State the blood parasite species.
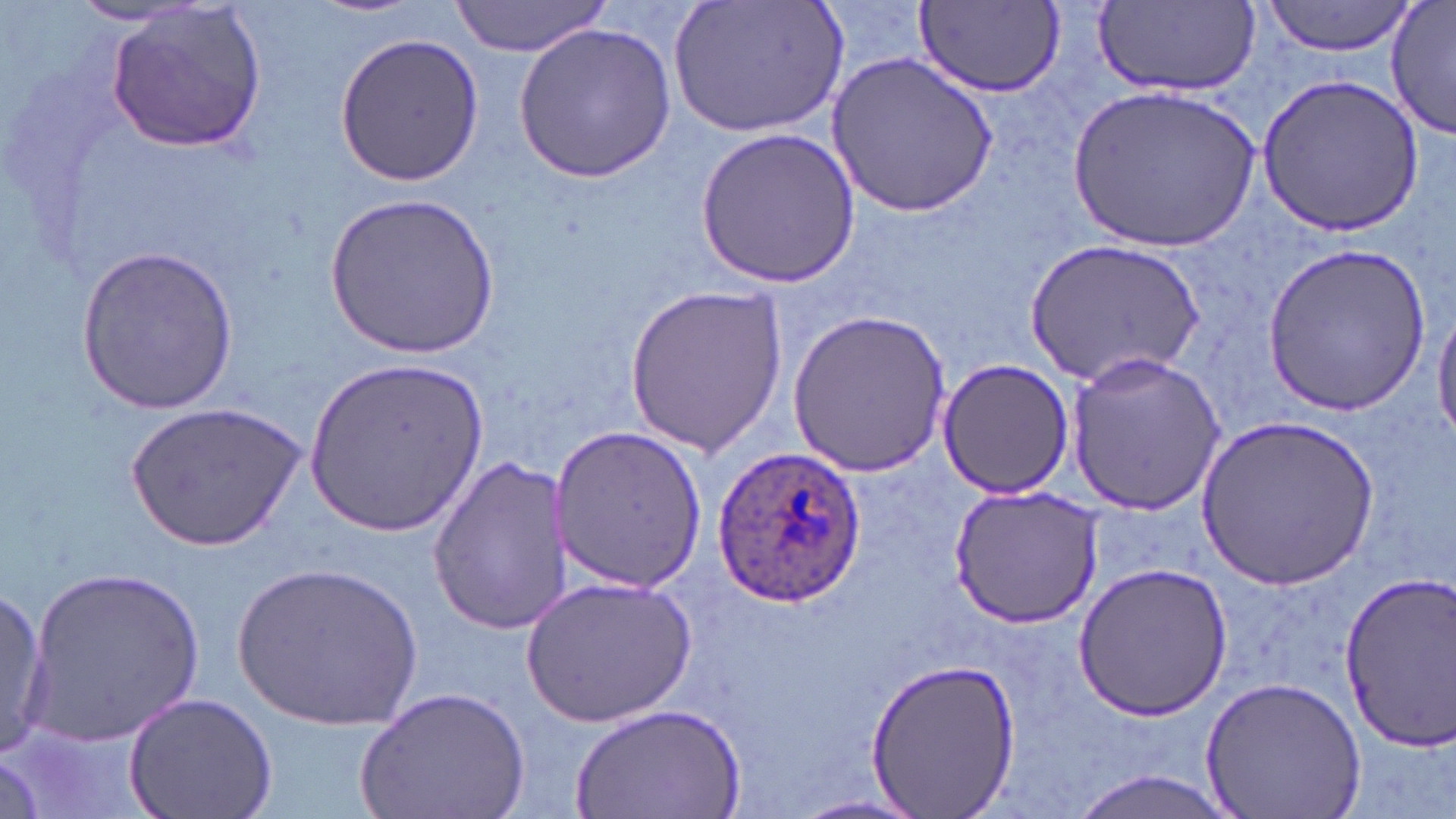
Plasmodium ovale.

Summary:
  - Coordinate format: approximate bounding boxes as named x1/y1/x2/y2 corners in pixels
  - Plasmodium ovale-infected red blood cell locations: (x1=708, y1=446, x2=869, y2=610)
  - Uninfected red blood cell locations: (x1=310, y1=0, x2=426, y2=18), (x1=664, y1=0, x2=847, y2=138), (x1=1260, y1=0, x2=1417, y2=57), (x1=449, y1=1, x2=613, y2=57), (x1=916, y1=2, x2=1063, y2=96), (x1=1092, y1=3, x2=1259, y2=96), (x1=68, y1=4, x2=202, y2=25), (x1=1386, y1=4, x2=1455, y2=140), (x1=107, y1=5, x2=268, y2=151), (x1=513, y1=24, x2=676, y2=182), (x1=334, y1=30, x2=485, y2=188), (x1=826, y1=52, x2=997, y2=216), (x1=1257, y1=72, x2=1425, y2=236), (x1=1068, y1=85, x2=1259, y2=254), (x1=694, y1=128, x2=858, y2=289), (x1=326, y1=191, x2=503, y2=357), (x1=1027, y1=239, x2=1203, y2=388), (x1=1262, y1=241, x2=1429, y2=415), (x1=76, y1=245, x2=238, y2=415), (x1=625, y1=282, x2=786, y2=454), (x1=1433, y1=303, x2=1456, y2=448), (x1=786, y1=308, x2=952, y2=480), (x1=1063, y1=352, x2=1226, y2=515), (x1=938, y1=358, x2=1072, y2=500), (x1=303, y1=359, x2=486, y2=536), (x1=124, y1=402, x2=306, y2=552), (x1=1197, y1=415, x2=1380, y2=591), (x1=553, y1=423, x2=708, y2=593), (x1=425, y1=458, x2=574, y2=632), (x1=950, y1=485, x2=1103, y2=627), (x1=234, y1=560, x2=422, y2=734), (x1=26, y1=562, x2=206, y2=745), (x1=1073, y1=562, x2=1232, y2=720), (x1=1334, y1=570, x2=1456, y2=747), (x1=521, y1=575, x2=697, y2=728), (x1=0, y1=587, x2=50, y2=759), (x1=862, y1=657, x2=1024, y2=818), (x1=1202, y1=674, x2=1367, y2=819), (x1=354, y1=682, x2=530, y2=819), (x1=122, y1=691, x2=278, y2=819), (x1=570, y1=702, x2=745, y2=819), (x1=1066, y1=768, x2=1244, y2=819), (x1=787, y1=794, x2=933, y2=819)
  - Modality: light microscopy
  - Preparation: thin blood film
  - Field of view: single
  - Stain: May-Grünwald-Giemsa
  - Magnification: 1000x
  - Image size: 1456×819 pixels